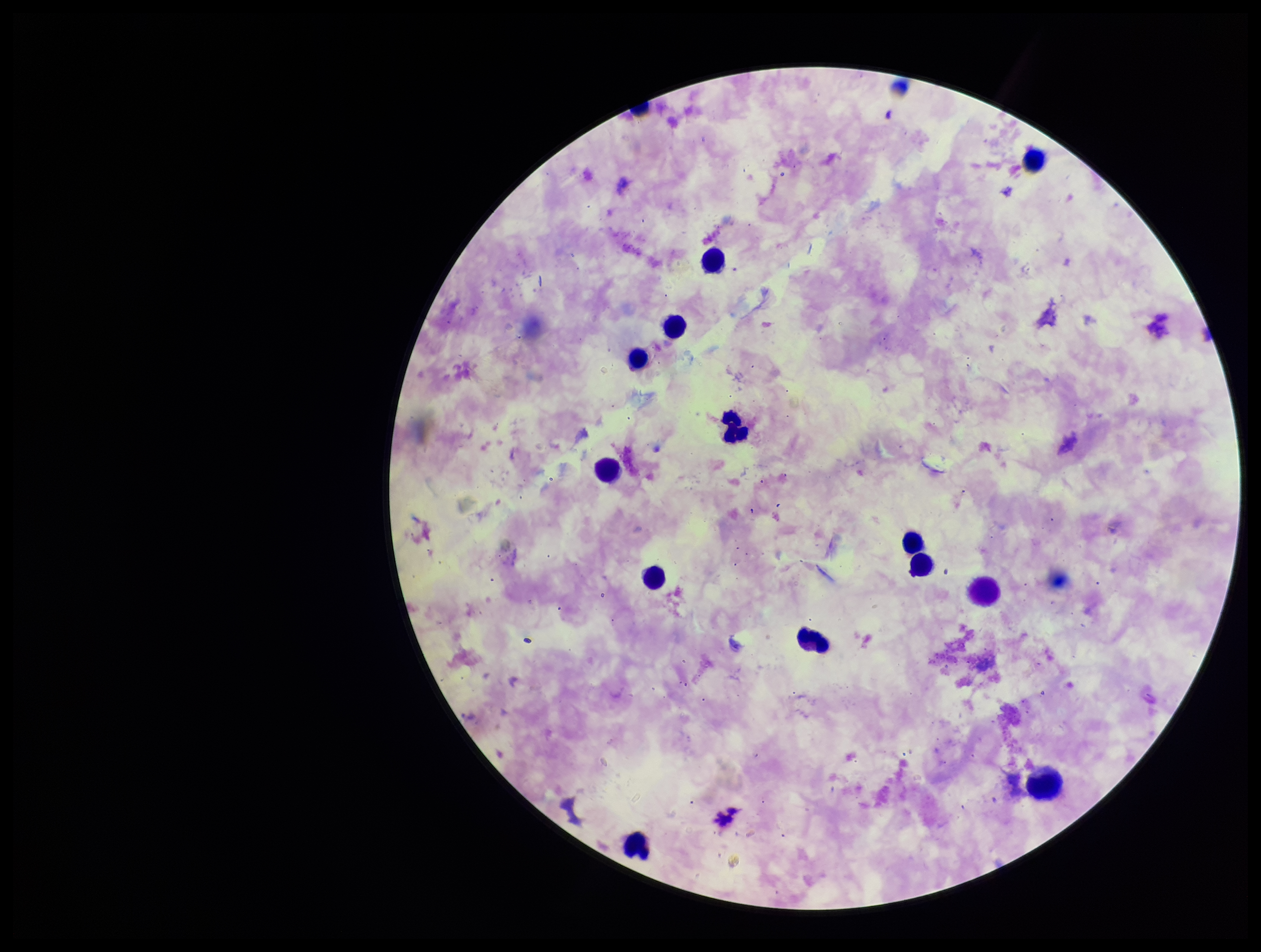
leukocyte count = 13
preparation = thick blood smear
patient malaria status = infected
field of view = single
Plasmodium parasites = none detected
image size = 1261×952 pixels
species reported for this patient = Plasmodium falciparum
capture = smartphone photograph through the microscope eyepiece
parasite count = 0
stain = Giemsa